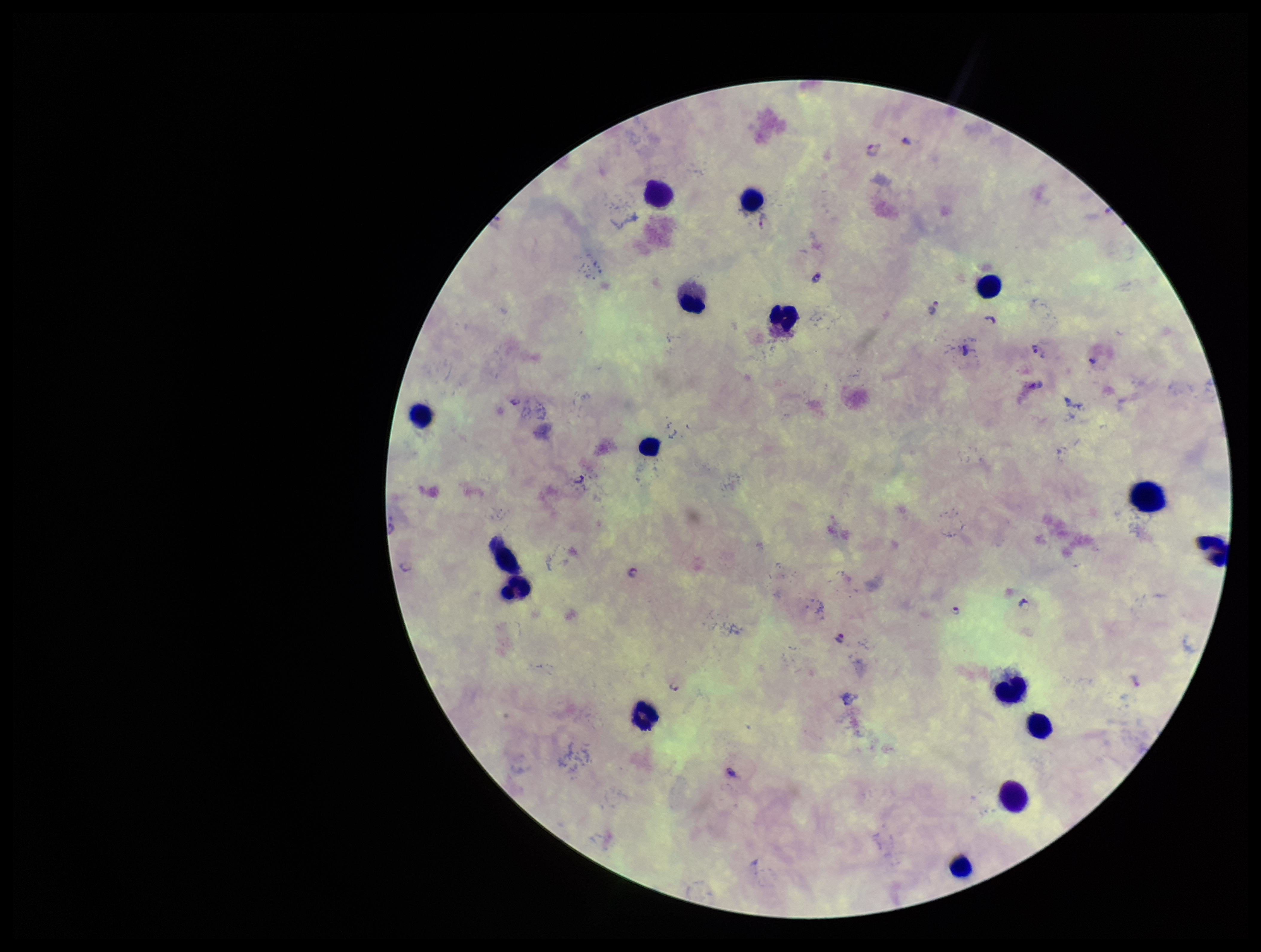

capture = smartphone photograph through the microscope eyepiece
field of view = one from this slide
image size = 1261×952 pixels
patient malaria status = positive
Plasmodium parasites = detected
parasite count = 7
stain = Giemsa
species reported for this patient = Plasmodium falciparum
leukocyte count = 16
preparation = thick blood smear